Assess this cell for malaria.
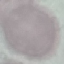

It is uninfected.

Summary:
  - Image type: cell patch, automatically extracted from a larger field of view and resized to 64 × 64 pixels
  - Preparation: thin smear
  - Capture: smartphone through the microscope eyepiece
  - Stain: Giemsa